Locate and identify every blood parasite.
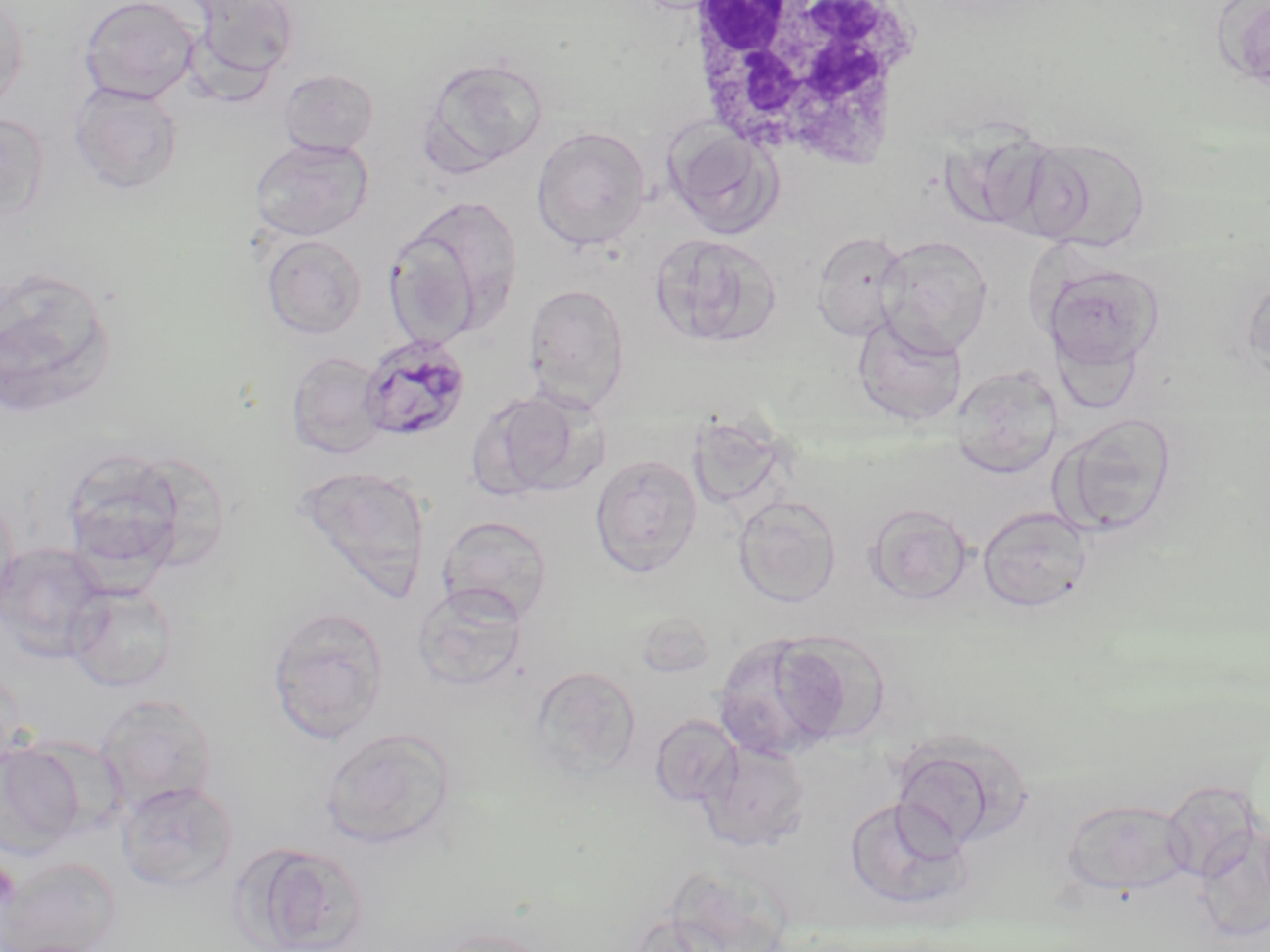

Approximate bounding boxes as [x1, y1, x2, y2] in pixels.
Plasmodium malariae-infected red blood cells: [359, 333, 471, 442].
No Plasmodium falciparum, Plasmodium ovale, Plasmodium vivax, Babesia divergens, or Trypanosoma brucei observed.

Platelet locations: [0, 861, 20, 913]. White blood cell locations: [677, 0, 927, 171]. Uninfected red blood cell locations: [0, 0, 29, 113], [79, 0, 201, 103], [187, 0, 300, 88], [1219, 0, 1269, 92], [417, 56, 549, 176], [278, 68, 380, 157], [70, 83, 184, 194], [0, 110, 49, 223], [663, 120, 784, 239], [943, 124, 1064, 235], [531, 126, 651, 250], [250, 136, 373, 241], [1020, 136, 1152, 252], [391, 194, 524, 340], [649, 232, 781, 350], [811, 232, 909, 342], [261, 234, 367, 339], [876, 235, 993, 356], [1041, 263, 1164, 373], [0, 265, 117, 421], [1242, 273, 1270, 390], [522, 283, 631, 410], [852, 315, 966, 426], [286, 351, 388, 460], [952, 364, 1063, 479], [471, 388, 602, 501], [687, 410, 791, 513], [1054, 414, 1179, 537], [59, 447, 195, 581], [589, 453, 703, 577], [296, 465, 432, 600], [0, 491, 21, 622], [733, 495, 841, 607], [865, 503, 974, 606], [977, 504, 1093, 613], [437, 515, 554, 624], [0, 542, 111, 663], [66, 582, 178, 692], [412, 584, 528, 689], [266, 606, 390, 744], [634, 610, 718, 678], [712, 632, 849, 760], [776, 639, 898, 735], [0, 663, 25, 780], [529, 666, 642, 781], [96, 693, 218, 813], [649, 714, 742, 806], [321, 728, 456, 849], [891, 733, 1029, 851], [698, 739, 811, 851], [0, 742, 86, 855], [117, 780, 239, 894], [1160, 781, 1266, 886], [845, 795, 972, 911], [1061, 798, 1194, 896], [237, 842, 369, 952], [3, 858, 122, 951], [428, 927, 558, 952]. Slide-level diagnosis: Plasmodium malariae. May-Grünwald-Giemsa stain. Image is 1270×952 pixels. 1000x magnification. Thin blood film. Single field of view. Light microscopy.